Report the malaria status of this cell.
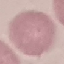
Uninfected.

Summary:
  - Preparation: thin blood smear
  - Stain: Giemsa
  - Capture: smartphone through the microscope eyepiece
  - Image type: automatically extracted cell patch, resized to 64 × 64 pixels